Comment on the morphology of the red blood cells.
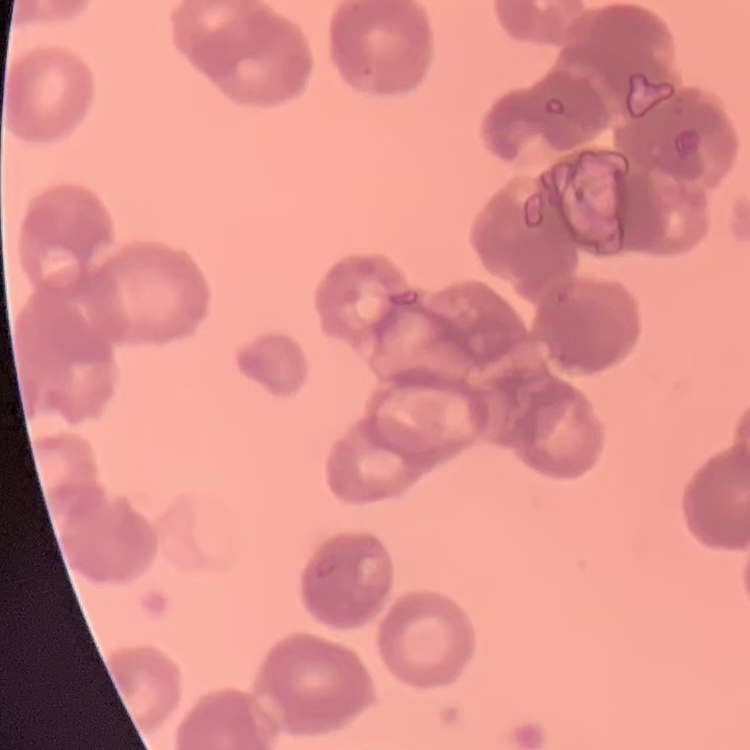
They show rouleaux formation.

stain = Field's or Giemsa
image type = one tile cut from a larger photomicrograph
preparation = thin peripheral smear